Assess this cell for malaria.
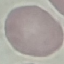

Uninfected.

Photographed with a smartphone camera at the microscope eyepiece. Cell patch, automatically extracted from a larger field of view and resized to 64 × 64 pixels. Thin blood film. Giemsa-stained preparation.